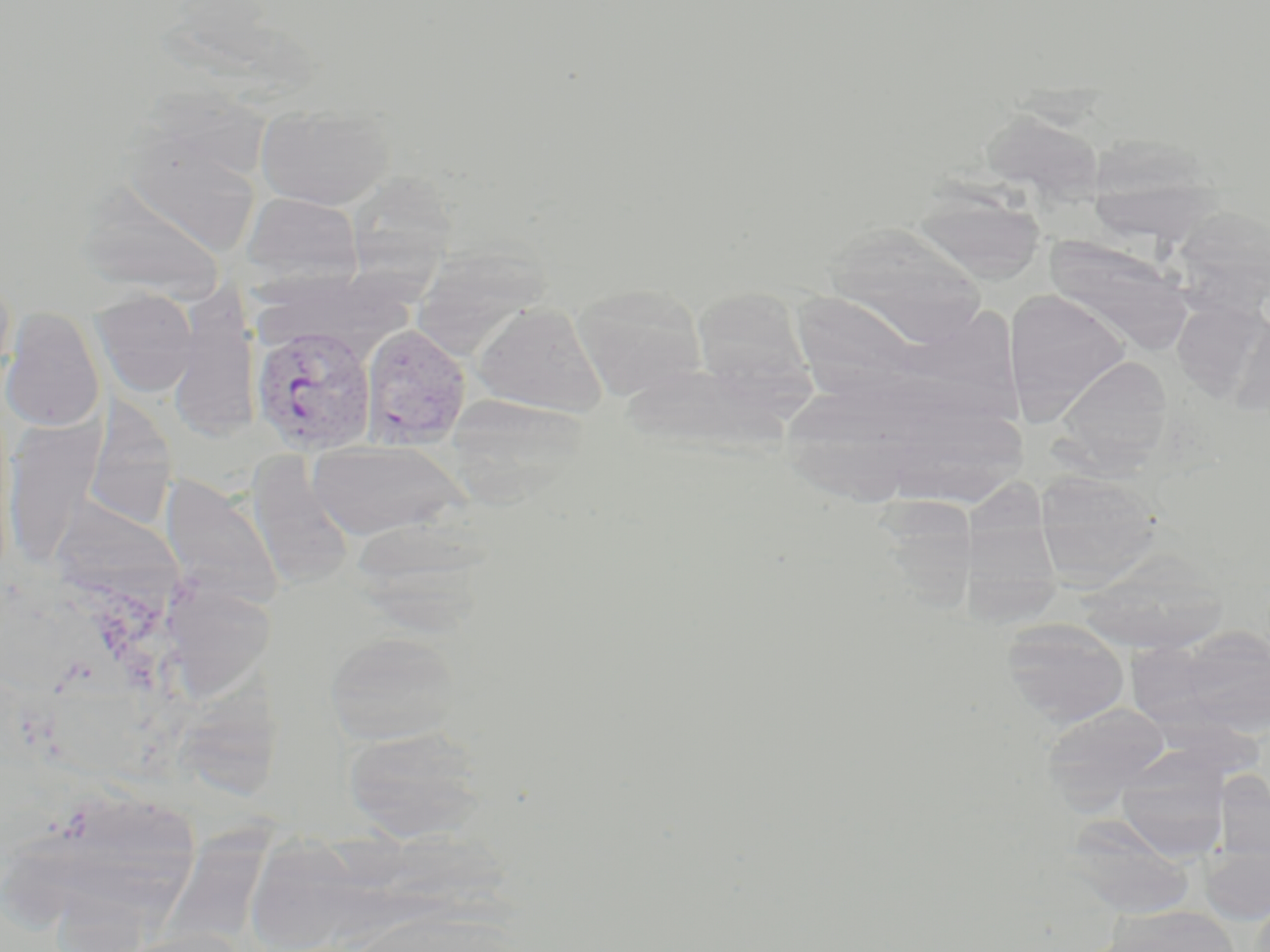

Approximate bounding boxes as (x1, y1, x2, y2) in pixels. Plasmodium vivax-infected red blood cell locations: (250, 325, 377, 455), (359, 328, 471, 453). Uninfected red blood cell locations: (255, 102, 394, 210), (121, 125, 263, 258), (1086, 143, 1224, 250), (350, 172, 453, 307), (74, 181, 229, 301), (241, 191, 365, 290), (912, 191, 1044, 284), (1168, 204, 1270, 318), (824, 223, 988, 349), (1045, 236, 1192, 353), (423, 240, 557, 353), (0, 258, 16, 396), (570, 282, 708, 401), (691, 287, 813, 402), (92, 288, 199, 397), (1002, 288, 1131, 423), (166, 292, 261, 442), (1171, 299, 1269, 400), (474, 302, 608, 417), (1, 307, 106, 432), (1229, 310, 1270, 415), (1053, 355, 1173, 474), (619, 361, 798, 455), (83, 398, 177, 531), (3, 416, 105, 567), (307, 441, 466, 541), (247, 455, 356, 589), (961, 469, 1066, 630), (1033, 471, 1163, 587), (160, 472, 283, 609), (879, 484, 983, 610), (48, 494, 183, 598), (345, 516, 499, 627), (1077, 550, 1230, 653), (174, 588, 274, 696), (1001, 617, 1131, 728), (1161, 627, 1270, 739), (324, 629, 463, 746), (183, 660, 297, 804), (1039, 701, 1172, 807), (342, 725, 491, 842), (1116, 747, 1230, 859), (1065, 816, 1195, 918), (170, 822, 279, 949), (253, 824, 358, 952), (1200, 839, 1270, 925), (1106, 905, 1240, 952), (110, 928, 254, 952). Slide-level diagnosis: Plasmodium vivax. May-Grünwald-Giemsa-stained preparation. Optical microscopy. Thin blood film. Captured at 1000x magnification. Image is 1270×952 pixels. One field of a larger specimen.